Report the malaria status of this cell.
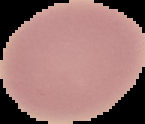
It is uninfected.

Segmented cell region on a black background. Image is 145×124 pixels. From a thin blood smear.